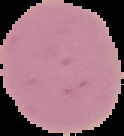

Summary:
  - Preparation: thin blood film
  - Image size: 124×136 pixels
  - Image type: segmented cell region with the area outside set to black
  - Malaria status: uninfected